Locate every Plasmodium parasite.
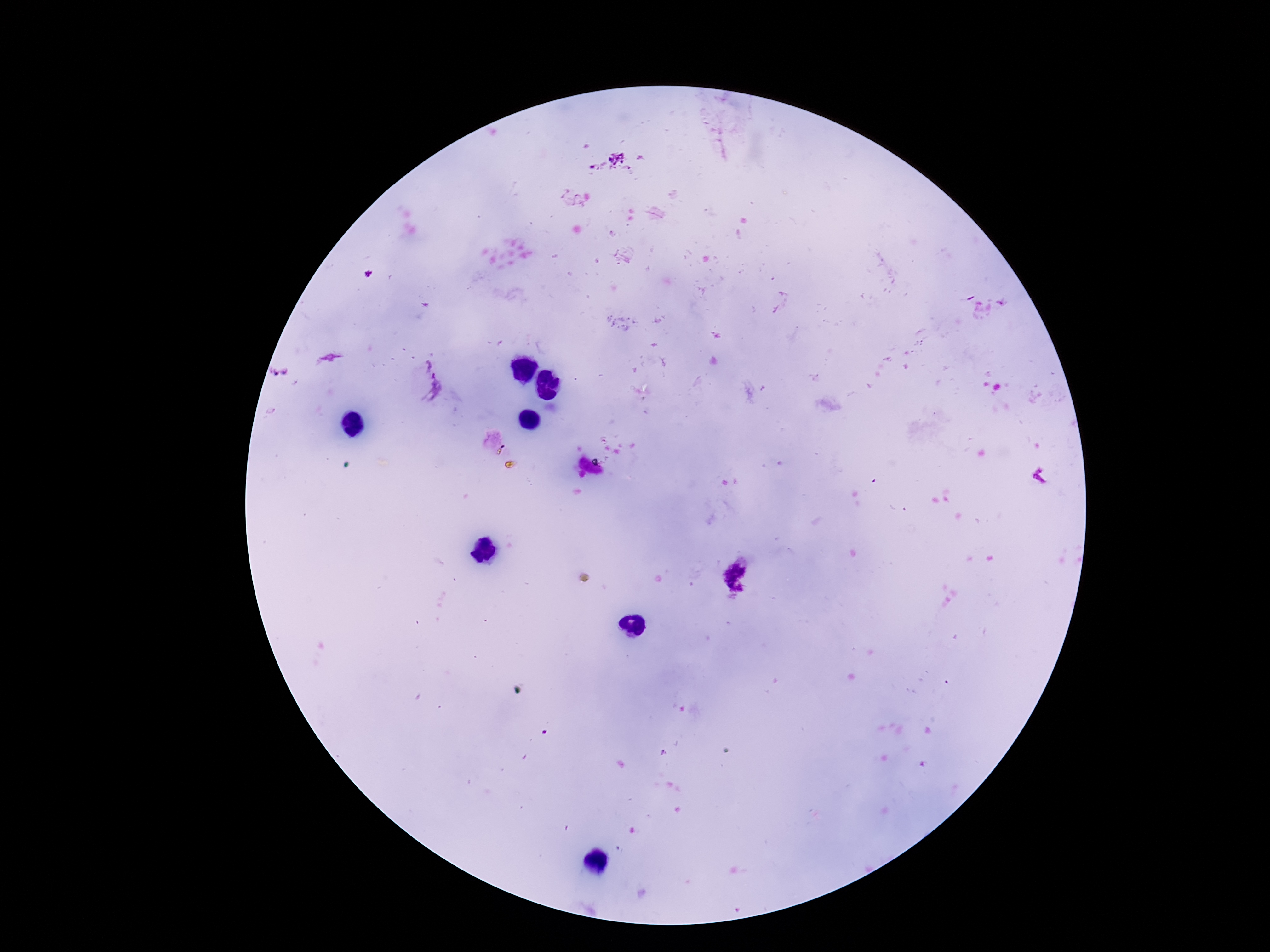

Approximate centers as (x, y) in pixels.
Plasmodium parasites: (369, 273), (427, 388).

capture = smartphone camera through the microscope eyepiece
patient malaria status = infected
preparation = thick blood smear
magnification = 100x
image size = 1270×952 pixels
stain = Giemsa
field of view = one from this slide